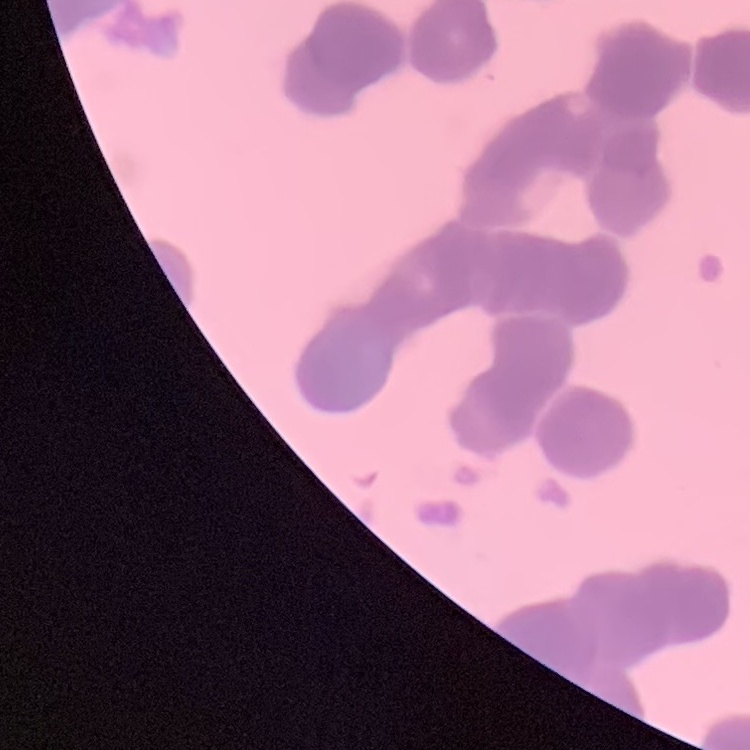 The erythrocytes show rouleaux formation. Field's or Giemsa stain. Square crop of a larger photomicrograph. Thin blood film.